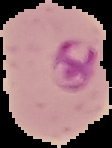
malaria_status: parasitized
image_type: segmented cell region with the area outside set to black
preparation: thin blood film
image_size: 112×148 pixels